Assess this cell for malaria.
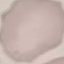
It is uninfected.

Summary:
  - Image type: cell patch, automatically extracted from a larger field of view and resized to 64 × 64 pixels
  - Stain: Giemsa
  - Capture: smartphone through the microscope eyepiece
  - Preparation: thin blood film